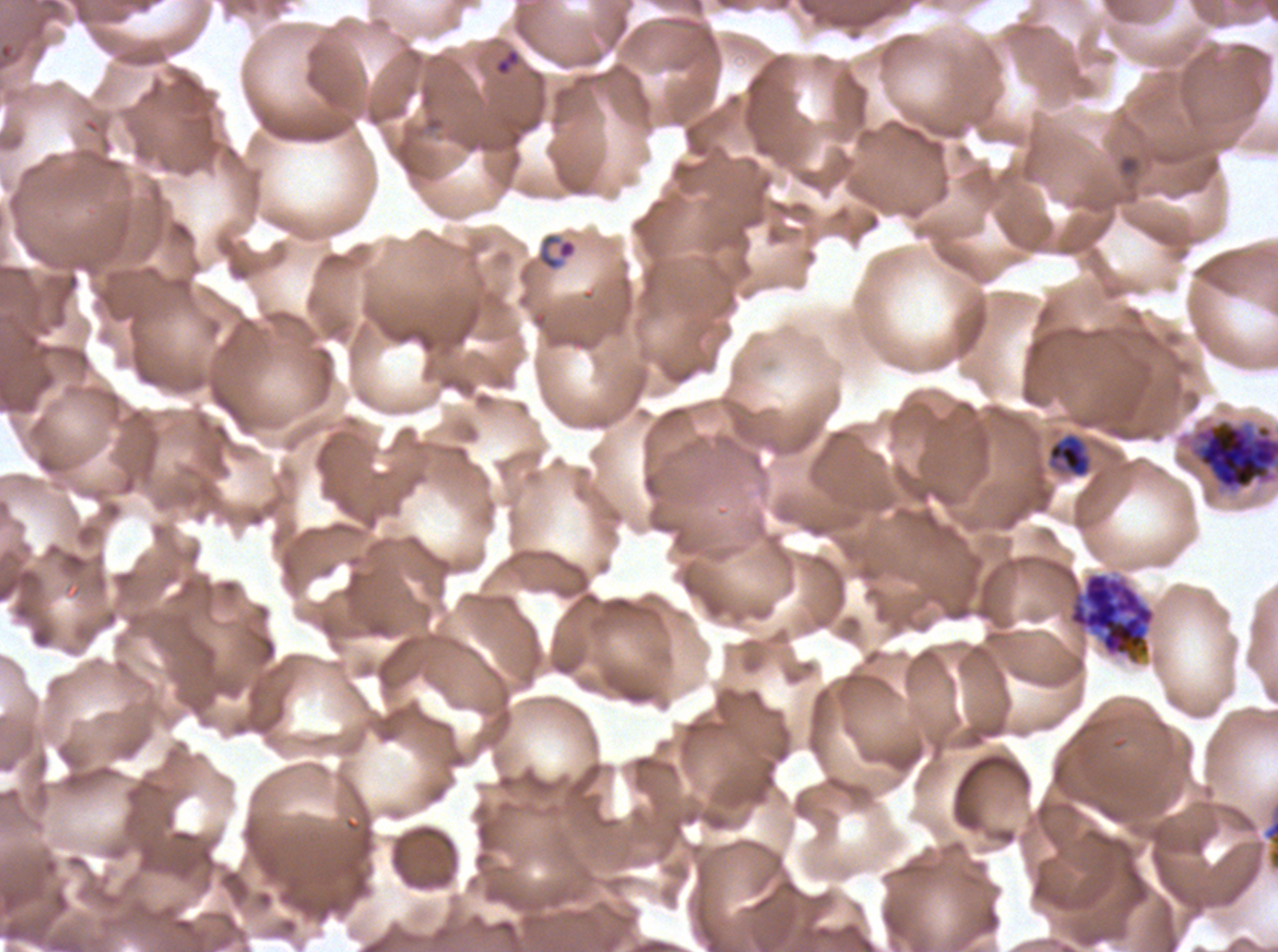
Approximate bounding rectangles given as corner coordinates in pixels from the top-left.
Summary:
  - Late schizont locations: (x1=1182, y1=418, x2=1277, y2=494)
  - Early schizont locations: (x1=1067, y1=571, x2=1157, y2=665)
  - Ring locations: (x1=494, y1=48, x2=521, y2=77), (x1=1116, y1=153, x2=1142, y2=178), (x1=537, y1=233, x2=578, y2=272)
  - Mid trophozoite locations: (x1=1047, y1=433, x2=1092, y2=479)
  - Field of view: sub-image separated from a larger composite
  - Life-cycle stages observed: ring, mid trophozoite, early schizont, late schizont
  - Specimen: Plasmodium falciparum cultured ex vivo for 24 to 48 hours, from a patient in The Gambia
  - Image size: 1278×952 pixels
  - Preparation: thin blood smear
  - Stain: Giemsa